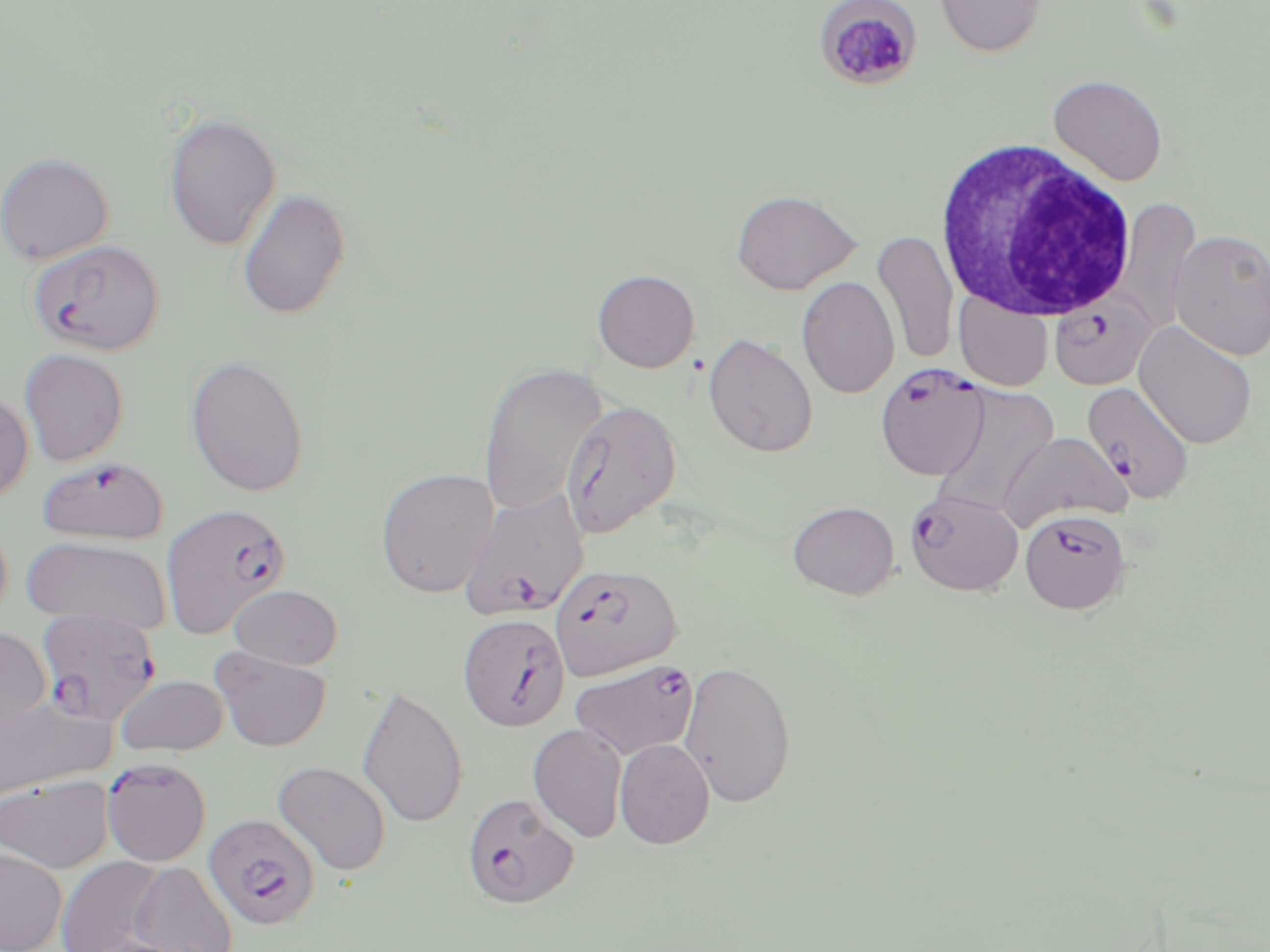
Approximate bounding boxes as named x1/y1/x2/y2 corners in pixels. Uninfected red blood cell locations (subset): (x1=934, y1=0, x2=1048, y2=58), (x1=1048, y1=73, x2=1169, y2=186), (x1=162, y1=112, x2=282, y2=251), (x1=0, y1=152, x2=114, y2=265), (x1=236, y1=188, x2=351, y2=320), (x1=731, y1=189, x2=862, y2=295), (x1=1112, y1=196, x2=1201, y2=337), (x1=1169, y1=229, x2=1270, y2=362), (x1=873, y1=230, x2=959, y2=365), (x1=592, y1=269, x2=700, y2=373), (x1=796, y1=275, x2=900, y2=399), (x1=954, y1=292, x2=1053, y2=392), (x1=1134, y1=320, x2=1258, y2=449), (x1=703, y1=333, x2=819, y2=458), (x1=18, y1=348, x2=129, y2=467), (x1=185, y1=354, x2=310, y2=498), (x1=477, y1=362, x2=608, y2=517), (x1=929, y1=383, x2=1060, y2=518), (x1=0, y1=390, x2=34, y2=505), (x1=560, y1=399, x2=682, y2=540), (x1=999, y1=432, x2=1131, y2=531), (x1=375, y1=468, x2=499, y2=598), (x1=787, y1=500, x2=899, y2=600), (x1=21, y1=536, x2=171, y2=632), (x1=230, y1=584, x2=343, y2=669), (x1=0, y1=626, x2=52, y2=744), (x1=210, y1=647, x2=331, y2=752), (x1=678, y1=658, x2=797, y2=808), (x1=114, y1=674, x2=229, y2=757), (x1=357, y1=684, x2=468, y2=830), (x1=0, y1=696, x2=114, y2=801), (x1=528, y1=723, x2=628, y2=843), (x1=614, y1=738, x2=715, y2=849), (x1=273, y1=760, x2=392, y2=876), (x1=0, y1=774, x2=114, y2=874), (x1=0, y1=846, x2=68, y2=952), (x1=56, y1=856, x2=170, y2=952), (x1=128, y1=860, x2=238, y2=952). White blood cell locations: (x1=936, y1=139, x2=1138, y2=324). Plasmodium falciparum-infected red blood cell locations (subset): (x1=28, y1=238, x2=164, y2=356), (x1=1049, y1=295, x2=1157, y2=391), (x1=875, y1=363, x2=989, y2=481), (x1=1082, y1=381, x2=1195, y2=504), (x1=36, y1=456, x2=169, y2=545), (x1=904, y1=488, x2=1024, y2=597), (x1=458, y1=489, x2=589, y2=621), (x1=1020, y1=508, x2=1132, y2=614), (x1=550, y1=564, x2=682, y2=681), (x1=36, y1=608, x2=163, y2=726), (x1=458, y1=612, x2=571, y2=732), (x1=569, y1=658, x2=699, y2=760), (x1=101, y1=759, x2=211, y2=866), (x1=462, y1=793, x2=580, y2=910), (x1=204, y1=814, x2=322, y2=931). Slide-level diagnosis: Plasmodium falciparum. Thin blood film. May-Grünwald-Giemsa-stained preparation. 1000x magnification. One field of a larger specimen. Light microscopy. Image is 1270×952 pixels.